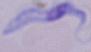
magnification = 1000x
identification = trypanosome
modality = photomicrograph